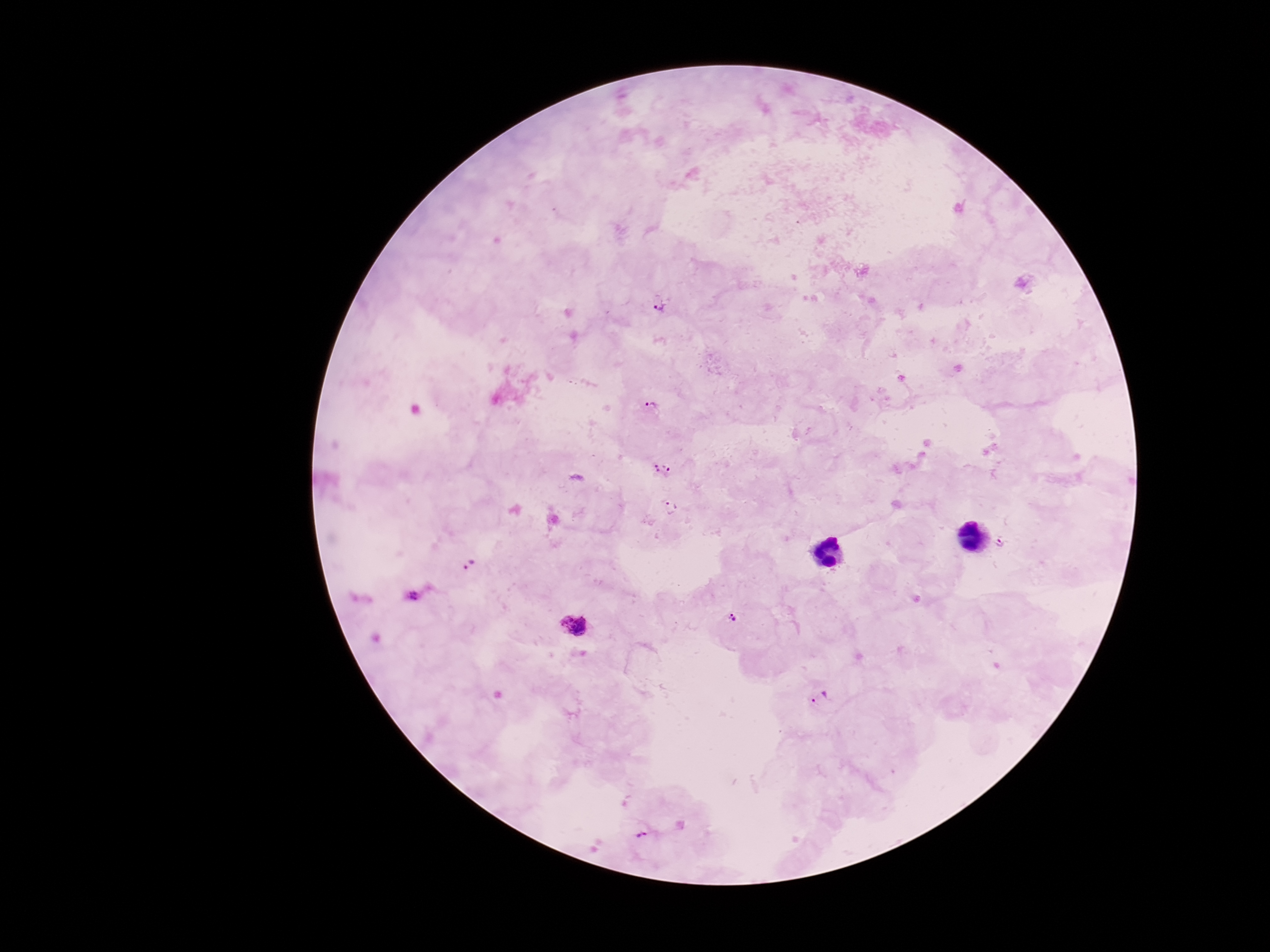

Approximate centers as {x, y} in pixels.
Summary:
  - Plasmodium parasite locations: {659, 304}, {652, 407}, {655, 468}, {669, 468}, {671, 507}, {1000, 543}, {469, 564}, {415, 596}, {733, 619}, {576, 625}, {819, 698}, {642, 835}
  - Capture: smartphone camera through the microscope eyepiece
  - Stain: Giemsa
  - Patient malaria status: infected
  - Magnification: 100x
  - Preparation: thick blood film
  - Field of view: one from this slide
  - Image size: 1270×952 pixels